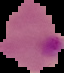

Summary:
  - Preparation: thin blood film
  - Image size: 64×73 pixels
  - Result: malaria parasites detected
  - Image type: cell region segmented out of the field of view; surrounding area masked to black